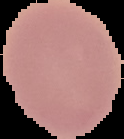
{
  "preparation": "thin blood film",
  "image_type": "segmented cell region on a black background",
  "result": "no Plasmodium parasites detected",
  "image_size": "124×139 pixels"
}